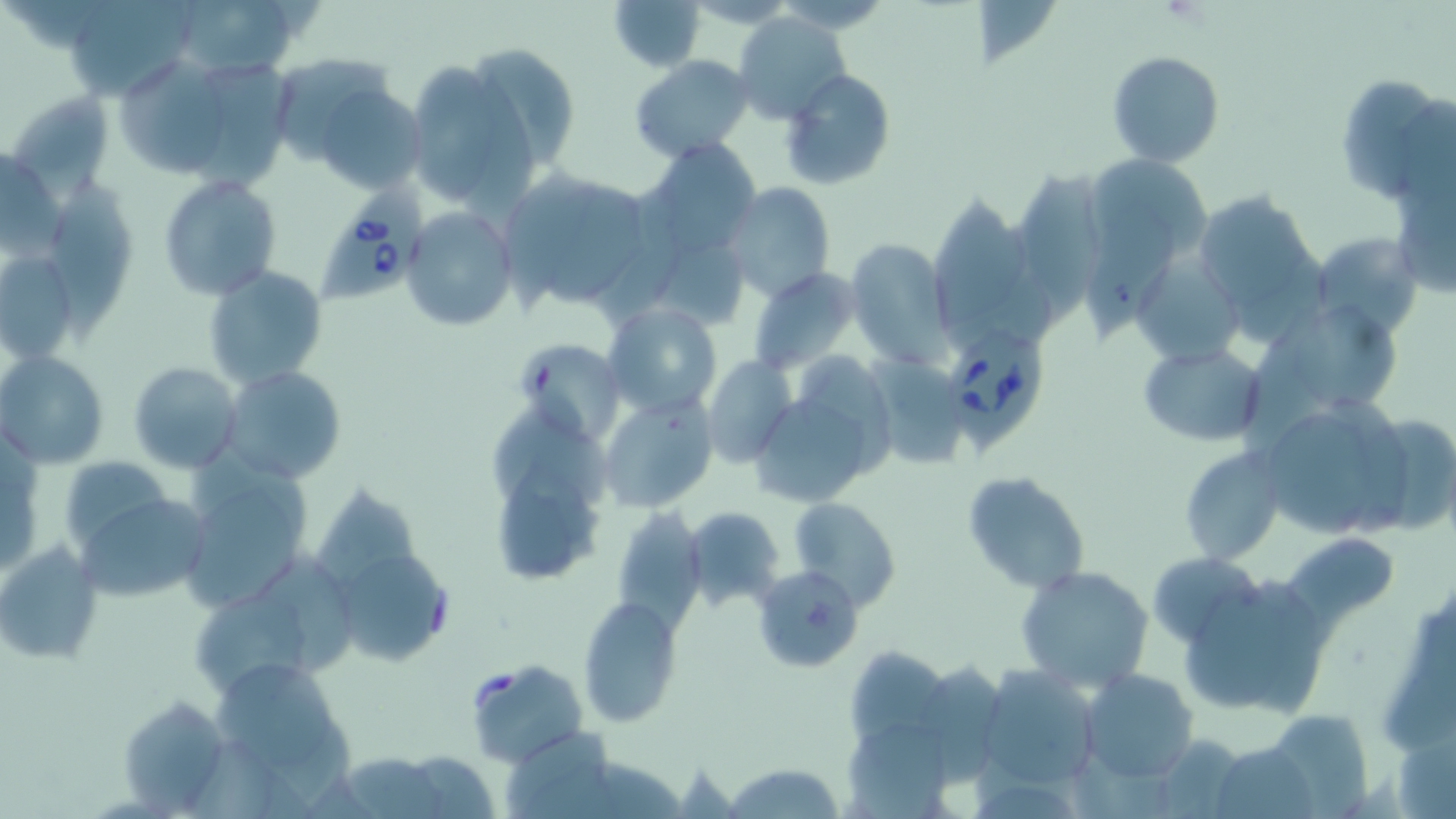
Approximate bounding boxes as named x1/y1/x2/y2 corners in pixels. Uninfected red blood cell locations: (x1=168, y1=0, x2=303, y2=80), (x1=606, y1=0, x2=711, y2=71), (x1=64, y1=1, x2=193, y2=100), (x1=970, y1=2, x2=1065, y2=67), (x1=734, y1=13, x2=851, y2=125), (x1=465, y1=40, x2=583, y2=176), (x1=1106, y1=50, x2=1225, y2=168), (x1=630, y1=55, x2=754, y2=163), (x1=115, y1=56, x2=225, y2=176), (x1=201, y1=56, x2=296, y2=197), (x1=285, y1=58, x2=400, y2=158), (x1=400, y1=62, x2=533, y2=207), (x1=780, y1=69, x2=896, y2=190), (x1=1342, y1=78, x2=1435, y2=195), (x1=317, y1=86, x2=424, y2=192), (x1=6, y1=89, x2=114, y2=193), (x1=1397, y1=98, x2=1456, y2=205), (x1=638, y1=141, x2=764, y2=259), (x1=0, y1=151, x2=69, y2=258), (x1=1082, y1=152, x2=1211, y2=275), (x1=47, y1=168, x2=142, y2=345), (x1=1016, y1=170, x2=1104, y2=328), (x1=502, y1=173, x2=604, y2=312), (x1=157, y1=175, x2=282, y2=300), (x1=720, y1=181, x2=835, y2=302), (x1=552, y1=185, x2=643, y2=303), (x1=930, y1=186, x2=1021, y2=340), (x1=1193, y1=188, x2=1325, y2=338), (x1=593, y1=195, x2=683, y2=327), (x1=1398, y1=200, x2=1456, y2=294), (x1=1084, y1=205, x2=1178, y2=341), (x1=402, y1=207, x2=517, y2=333), (x1=1308, y1=230, x2=1423, y2=338), (x1=846, y1=238, x2=955, y2=369), (x1=656, y1=251, x2=747, y2=327), (x1=0, y1=254, x2=76, y2=360), (x1=1141, y1=265, x2=1242, y2=364), (x1=204, y1=266, x2=328, y2=388), (x1=748, y1=267, x2=858, y2=376), (x1=1252, y1=293, x2=1404, y2=421), (x1=604, y1=302, x2=721, y2=417), (x1=1245, y1=306, x2=1326, y2=466), (x1=518, y1=340, x2=626, y2=447), (x1=1138, y1=340, x2=1269, y2=449), (x1=2, y1=350, x2=108, y2=469), (x1=801, y1=355, x2=892, y2=476), (x1=871, y1=355, x2=963, y2=465), (x1=701, y1=356, x2=797, y2=467), (x1=129, y1=362, x2=244, y2=473), (x1=220, y1=365, x2=344, y2=483), (x1=599, y1=394, x2=718, y2=515), (x1=758, y1=398, x2=861, y2=508), (x1=491, y1=412, x2=609, y2=513), (x1=1356, y1=413, x2=1456, y2=533), (x1=1276, y1=419, x2=1376, y2=532), (x1=192, y1=447, x2=314, y2=544), (x1=1177, y1=447, x2=1285, y2=565), (x1=63, y1=456, x2=173, y2=552), (x1=496, y1=461, x2=594, y2=578), (x1=178, y1=464, x2=311, y2=611), (x1=960, y1=470, x2=1090, y2=595), (x1=308, y1=485, x2=427, y2=589), (x1=68, y1=486, x2=210, y2=604), (x1=789, y1=497, x2=900, y2=612), (x1=610, y1=506, x2=708, y2=629), (x1=683, y1=507, x2=783, y2=609), (x1=1283, y1=533, x2=1390, y2=636), (x1=0, y1=541, x2=102, y2=666), (x1=330, y1=545, x2=448, y2=668), (x1=1147, y1=551, x2=1266, y2=648), (x1=258, y1=552, x2=355, y2=680), (x1=1015, y1=564, x2=1154, y2=694), (x1=761, y1=566, x2=866, y2=671), (x1=1252, y1=580, x2=1321, y2=718), (x1=1187, y1=583, x2=1287, y2=705), (x1=190, y1=594, x2=316, y2=705), (x1=1389, y1=594, x2=1456, y2=755), (x1=579, y1=598, x2=680, y2=727), (x1=842, y1=647, x2=962, y2=788), (x1=465, y1=658, x2=587, y2=768), (x1=920, y1=660, x2=1007, y2=788), (x1=978, y1=665, x2=1102, y2=788), (x1=207, y1=666, x2=334, y2=769), (x1=1079, y1=666, x2=1200, y2=783), (x1=115, y1=695, x2=230, y2=813), (x1=1263, y1=708, x2=1371, y2=815), (x1=847, y1=722, x2=950, y2=819), (x1=507, y1=728, x2=608, y2=812), (x1=1395, y1=728, x2=1456, y2=819), (x1=1146, y1=733, x2=1248, y2=818), (x1=1209, y1=741, x2=1317, y2=819), (x1=402, y1=751, x2=497, y2=817), (x1=333, y1=753, x2=444, y2=818), (x1=528, y1=758, x2=688, y2=819), (x1=721, y1=762, x2=845, y2=818), (x1=978, y1=782, x2=1075, y2=819). Babesia divergens-infected red blood cell locations: (x1=315, y1=186, x2=429, y2=301), (x1=944, y1=320, x2=1044, y2=463). Slide-level diagnosis: Babesia divergens. Thin blood film. One field of a larger specimen. Image is 1456×819 pixels. 1000x magnification. May-Grünwald-Giemsa-stained preparation. Optical microscopy.